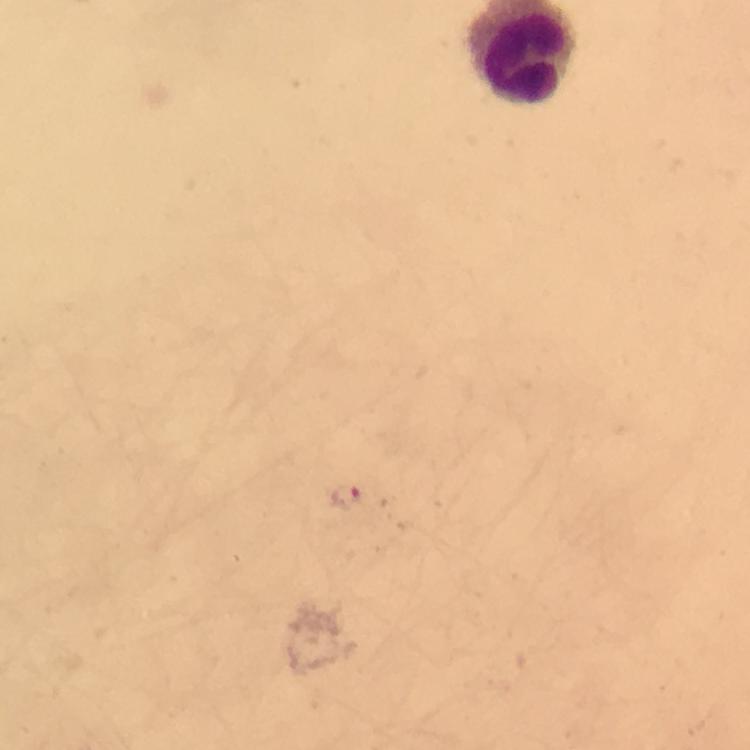
Approximate object centers, in pixels from the top-left corner. Plasmodium parasite locations: (x=347, y=495). Immersion oil was used. Giemsa-stained preparation. A crop from one field of view. From a diagnostic examination for malaria. Image is 750×750 pixels. Thick blood smear. Photographed with a smartphone mounted on the microscope. 100x magnification.